Report the malaria status of this cell.
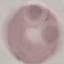
It is uninfected.

image type = automatically extracted cell patch, resized to 64 × 64 pixels
capture = smartphone through the microscope eyepiece
preparation = thin blood film
stain = Giemsa